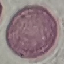
result = no malaria parasites seen
preparation = thin blood film
image type = cell patch, automatically extracted from a larger field of view and resized to 64 × 64 pixels
stain = Giemsa
capture = smartphone through the microscope eyepiece